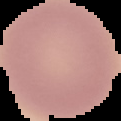
Malaria status: uninfected. Segmented cell region on a black background. Image is 121×121 pixels. From a thin blood smear.